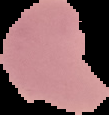
preparation = thin blood smear
image size = 109×115 pixels
malaria status = parasitized
image type = cell region segmented out of the field of view; surrounding area masked to black